Assess this cell for malaria.
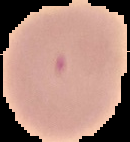
Parasitized.

Summary:
  - Image size: 130×142 pixels
  - Preparation: thin blood film
  - Image type: cell region segmented out of the field of view; surrounding area masked to black